Assess this cell for malaria.
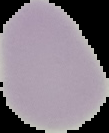
Uninfected.

The area outside the segmented cell region is set to black. Image is 109×133 pixels. From a thin blood film.